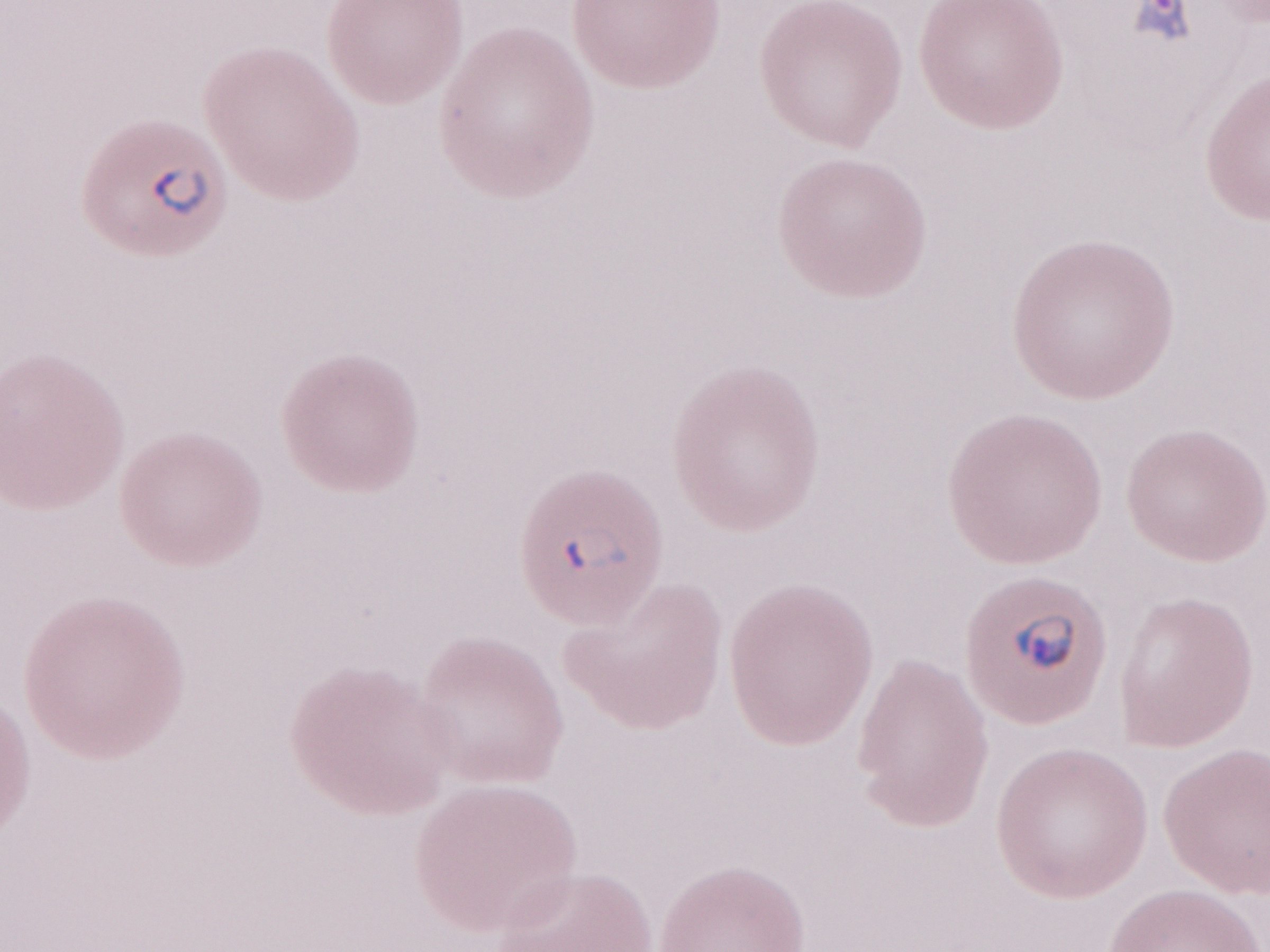 1,000x magnification. May-Grünwald-Giemsa (MGG) stain. One field of this slide. Malaria diagnosis (patient-level): positive. Thin peripheral-blood smear. Olympus BX43 microscope and DP73 digital camera. Image is 1270×952 pixels.